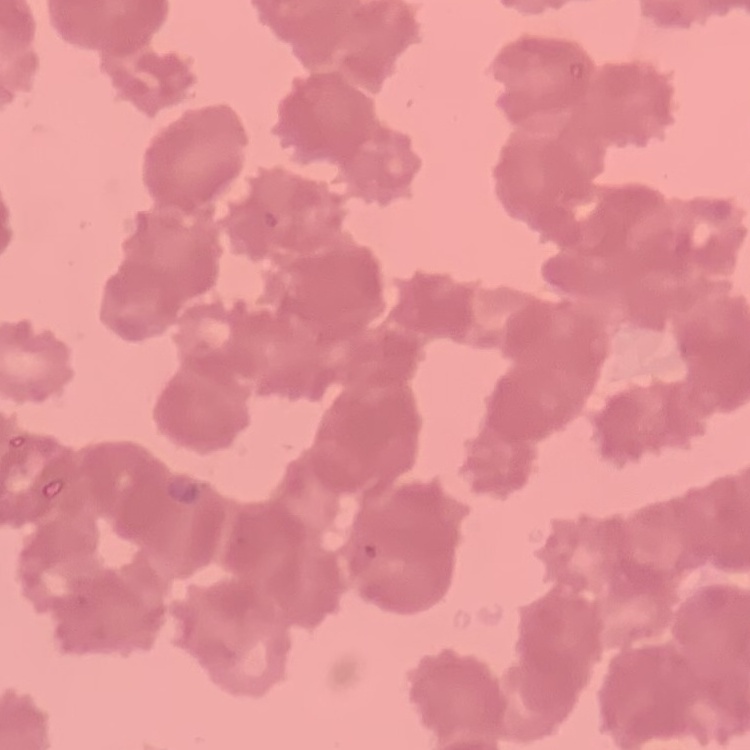

erythrocyte morphology = rouleaux formation
preparation = thin peripheral smear
stain = Field's or Giemsa
image type = one tile cut from a larger photomicrograph